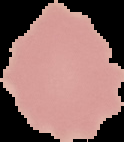 The area outside the segmented cell region is set to black. From a thin blood film. Image is 124×142 pixels. Malaria status: uninfected.